Classify this cell by malaria status.
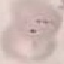

It is uninfected.

Photographed with a smartphone camera at the microscope eyepiece. Giemsa stain. Automatically extracted cell patch, resized to 64 × 64 pixels. Thin blood film.